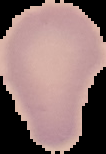
From a thin blood film. Image is 106×154 pixels. Malaria status: uninfected. Segmented cell region on a black background.